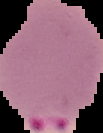

Malaria status: parasitized. Image is 103×133 pixels. From a thin blood film. Cell region segmented out of the field of view; the surrounding area is masked to black.